Give the extent of all uninfected red blood cells.
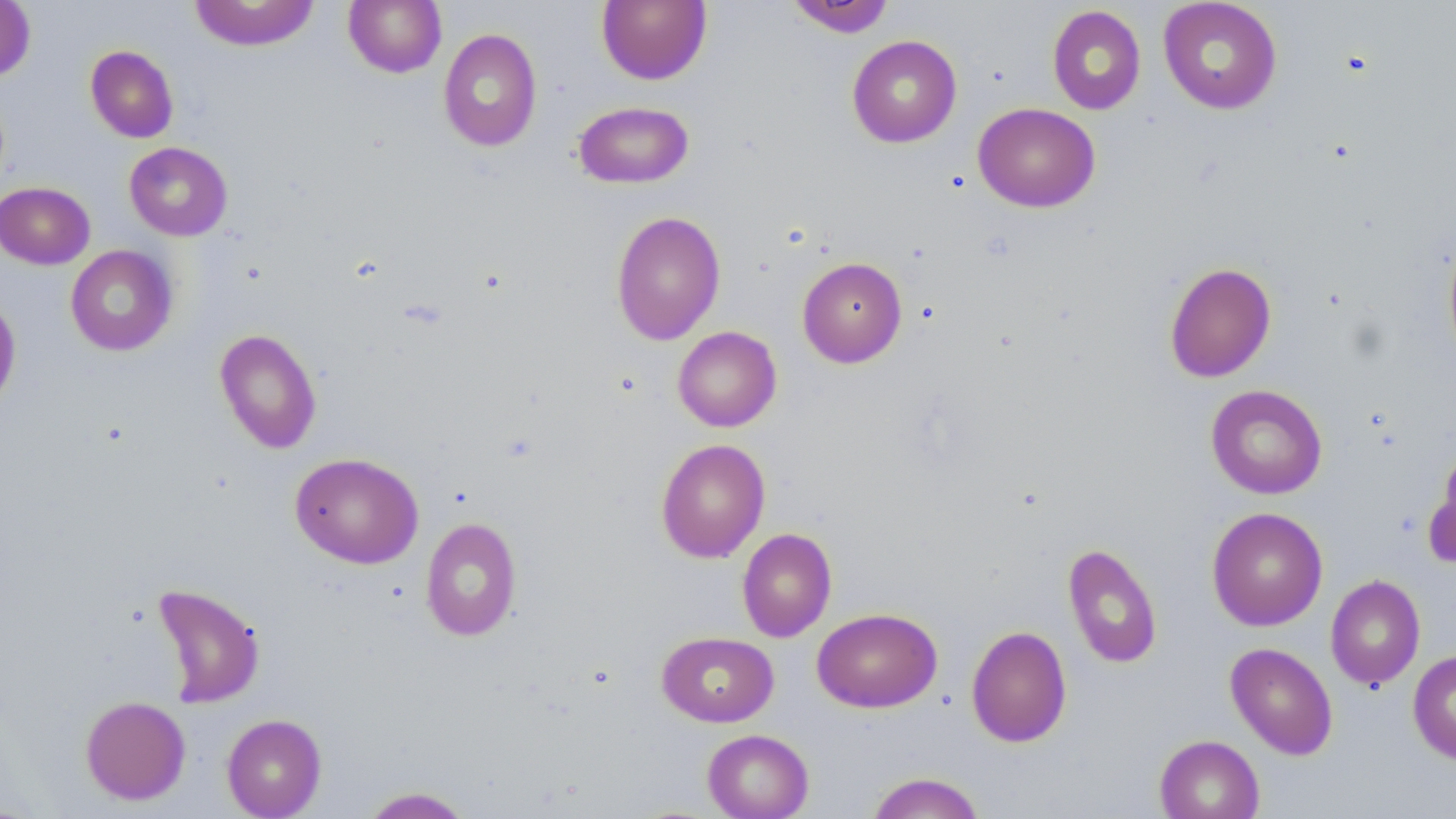
Approximate bounding boxes as (x1,y1)-(x2,y2) corner pairs in pixels.
Uninfected red blood cells: (189,0)-(320,51), (343,0)-(446,78), (596,0)-(712,85), (785,0)-(896,37), (1158,0)-(1282,115), (0,1)-(36,82), (1046,5)-(1146,115), (438,28)-(542,152), (847,35)-(962,148), (85,45)-(179,143), (573,100)-(694,189), (973,103)-(1100,213), (124,142)-(233,241), (0,181)-(95,270), (610,210)-(726,346), (1442,227)-(1456,366), (65,245)-(178,356), (797,257)-(907,367), (1164,261)-(1277,383), (0,292)-(21,413), (672,326)-(782,432), (214,328)-(322,454), (1205,384)-(1328,499), (655,438)-(771,563), (1425,450)-(1456,572), (290,452)-(424,569), (1207,506)-(1328,631), (421,517)-(522,641), (737,528)-(837,642), (1062,542)-(1163,669), (1325,574)-(1425,690), (151,583)-(266,709), (812,607)-(942,713), (965,625)-(1072,748), (657,631)-(779,727), (1225,642)-(1338,759), (1408,649)-(1456,765), (80,696)-(191,805), (221,713)-(327,819), (702,729)-(814,819), (1154,734)-(1265,819), (865,771)-(986,818), (359,786)-(474,818).

slide_level_diagnosis: negative for blood parasites
field_of_view: single
magnification: 1000x
preparation: thin blood smear
modality: optical microscopy
stain: May-Grünwald-Giemsa
image_size: 1456×819 pixels